Identify the parasite.
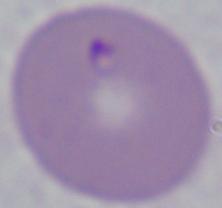

This is Babesia.

Summary:
  - Modality: micrograph
  - Magnification: 1000x